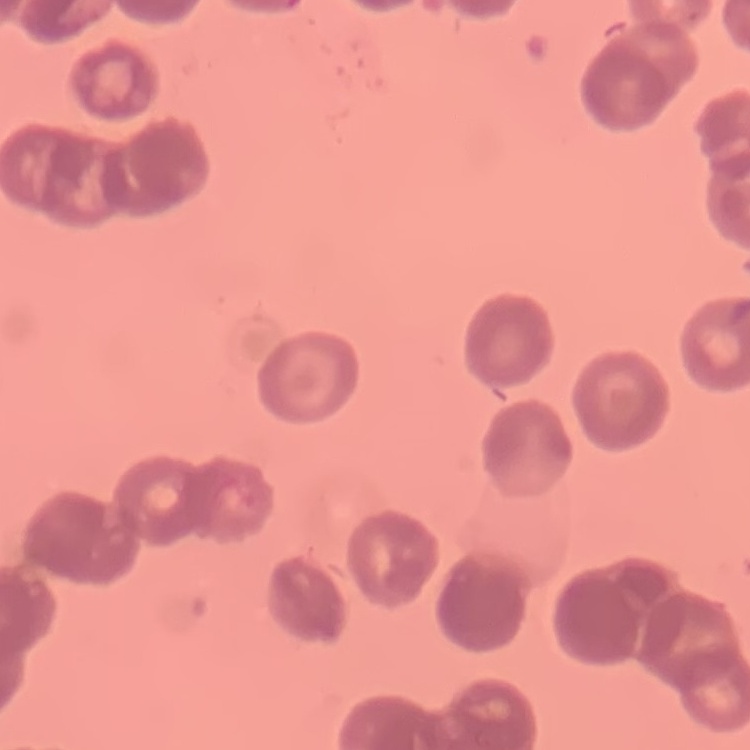 The red blood cells exhibit rouleaux formation. Square crop of a larger photomicrograph. Thin blood film. Stained with either Field's or Giemsa.